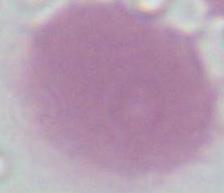
identification = erythrocyte
modality = photomicrograph
magnification = 1000x